Assess this cell for malaria.
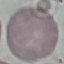
Uninfected.

Giemsa-stained preparation. Thin smear of blood. Cell patch, automatically extracted from a larger field of view and resized to 64 × 64 pixels. Acquired by smartphone through the microscope eyepiece.